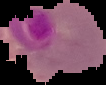

image_size: 106×85 pixels
preparation: thin blood smear
result: Plasmodium parasites detected
image_type: cell region segmented out of the field of view; surrounding area masked to black